Name the parasite shown.
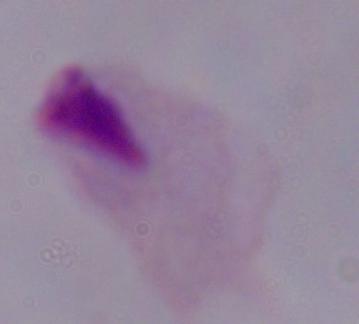

A trichomonad.

Summary:
  - Magnification: 1000x
  - Modality: photomicrograph